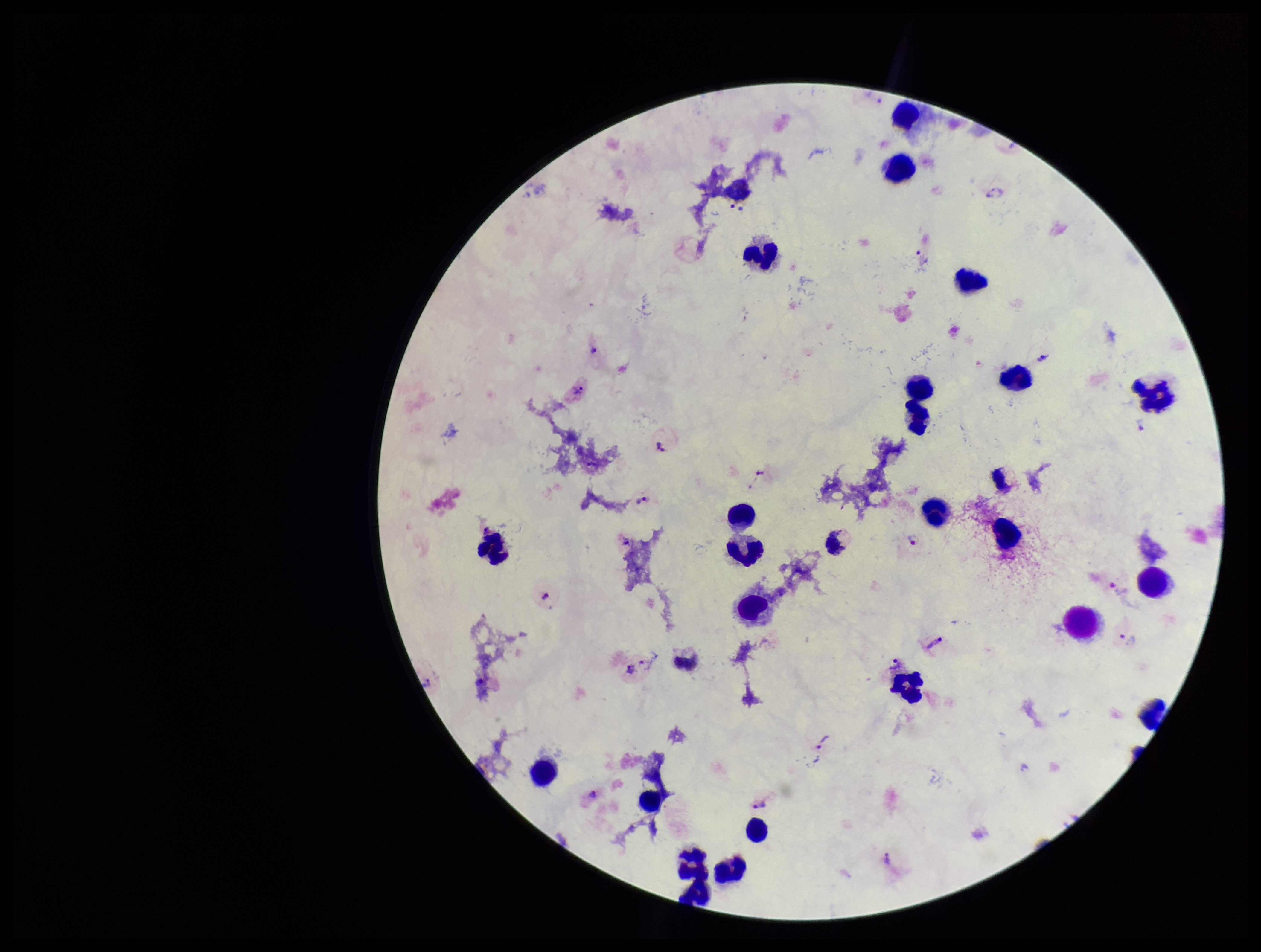
Summary:
  - Species reported for this patient: Plasmodium vivax
  - Parasite count: 8
  - Preparation: thick blood smear
  - Capture: smartphone photograph through the microscope eyepiece
  - Image size: 1261×952 pixels
  - Patient malaria status: infected
  - Leukocyte count: 26
  - Stain: Giemsa
  - Field of view: single
  - Plasmodium parasites: identified